Locate every malaria parasite by life-cycle stage, and every leukocyte.
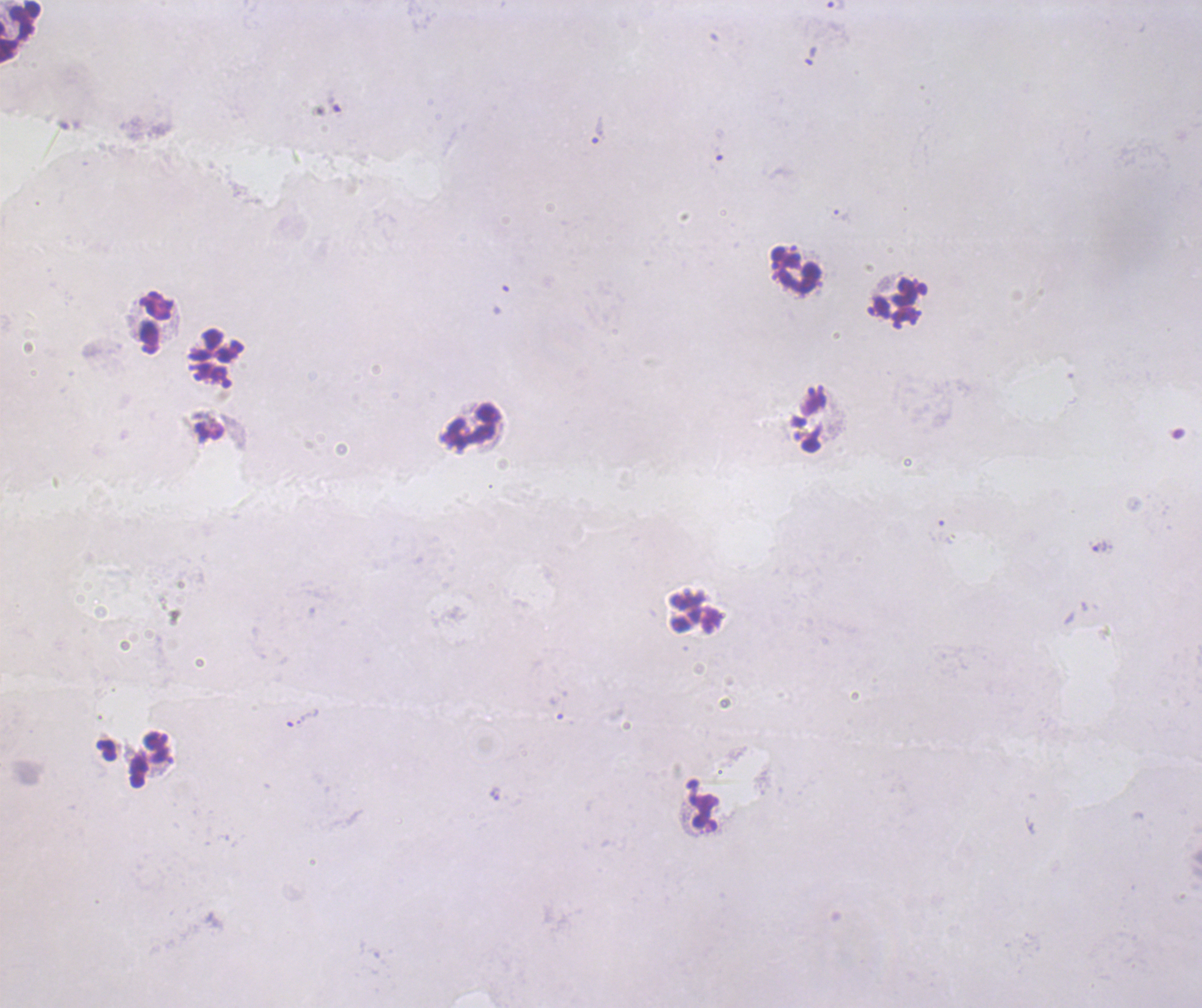

Approximate centers as [x, y] in pixels.
Trophozoites: [836, 6], [599, 130], [1099, 547].
No schizont or gametocyte forms observed.
Leukocytes: [19, 30], [795, 271], [898, 302], [154, 322], [216, 358], [470, 426], [697, 610].

Image is 1202×1008 pixels. One field from this slide. Coloration quality: bad. Captured at 100x magnification. Romanowsky stain. Previously used in an actual diagnosis. Thick smear of blood. Background quality: unsatisfactory.